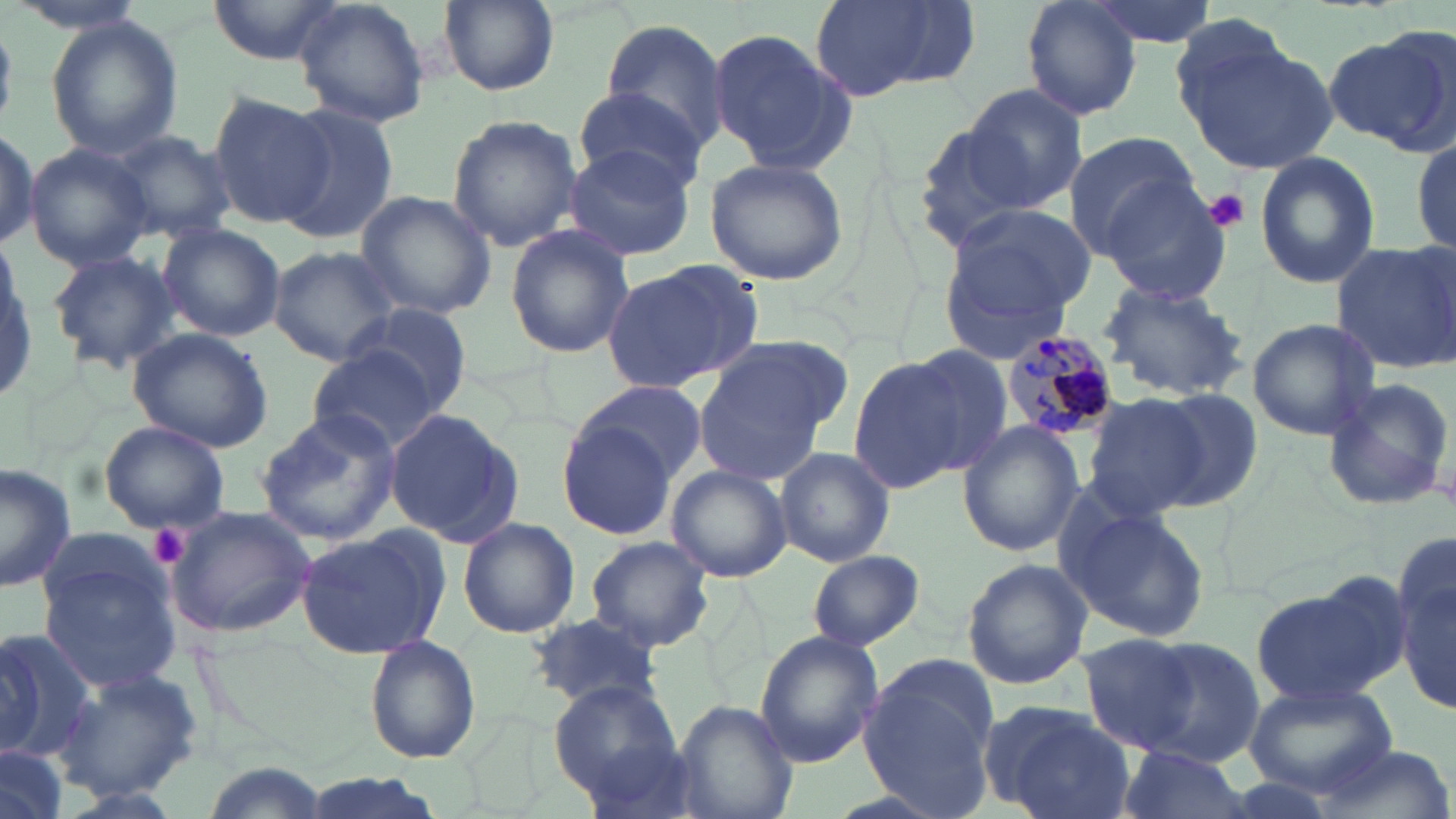
slide-level diagnosis = Plasmodium malariae
image size = 1456×819 pixels
magnification = 1000x
uninfected red blood cell locations = approximate bounding boxes as [x1, y1, x2, y2] in pixels: [211, 0, 337, 65], [293, 0, 431, 128], [1019, 0, 1144, 118], [1083, 0, 1217, 49], [437, 1, 558, 95], [809, 1, 977, 102], [45, 17, 184, 160], [595, 20, 732, 153], [707, 27, 857, 177], [1178, 27, 1337, 177], [1327, 27, 1456, 151], [963, 83, 1089, 212], [575, 86, 709, 194], [207, 91, 336, 229], [274, 105, 401, 245], [447, 115, 584, 252], [908, 118, 1041, 252], [0, 126, 38, 252], [1062, 130, 1206, 260], [108, 132, 235, 243], [1412, 136, 1455, 255], [562, 143, 696, 263], [25, 144, 153, 271], [1253, 152, 1381, 289], [703, 158, 850, 285], [1099, 181, 1235, 304], [354, 190, 498, 320], [949, 201, 1098, 314], [157, 224, 284, 342], [504, 225, 635, 358], [1331, 239, 1456, 373], [939, 243, 1076, 367], [267, 246, 404, 366], [44, 248, 182, 375], [601, 260, 761, 394], [1098, 281, 1249, 400], [349, 301, 475, 418], [1246, 317, 1383, 440], [128, 327, 274, 453], [690, 335, 848, 482], [908, 345, 1013, 475], [306, 347, 445, 453], [848, 355, 967, 495], [1321, 375, 1455, 512], [574, 378, 708, 488], [1149, 386, 1263, 510], [1080, 393, 1210, 520], [254, 407, 404, 547], [387, 410, 524, 550], [557, 417, 680, 540], [99, 420, 230, 533], [957, 421, 1084, 557], [773, 447, 894, 568], [0, 461, 79, 592], [666, 465, 792, 582], [1055, 496, 1211, 646], [165, 505, 316, 637], [458, 518, 581, 639], [295, 525, 449, 659], [584, 536, 714, 651], [37, 539, 186, 695], [807, 550, 925, 652], [1397, 550, 1454, 714], [962, 559, 1092, 689], [1252, 580, 1403, 708], [527, 611, 664, 711], [0, 629, 97, 764], [754, 631, 884, 767], [1077, 632, 1205, 755], [365, 635, 481, 764], [1136, 637, 1270, 763], [858, 653, 1002, 814], [54, 664, 200, 802], [549, 678, 685, 809], [1242, 678, 1398, 799], [672, 699, 797, 819], [984, 701, 1137, 819], [1114, 746, 1253, 819], [0, 747, 66, 819], [1311, 747, 1452, 819], [200, 759, 332, 819], [294, 771, 451, 819]
platelet locations = approximate bounding boxes as [x1, y1, x2, y2] in pixels: [1204, 189, 1250, 232], [147, 523, 190, 570]
Plasmodium malariae-infected red blood cell locations = approximate bounding boxes as [x1, y1, x2, y2] in pixels: [999, 329, 1118, 440]
stain = May-Grünwald-Giemsa
modality = light microscopy
preparation = thin blood smear
field of view = single